Locate every blood parasite and identify its species.
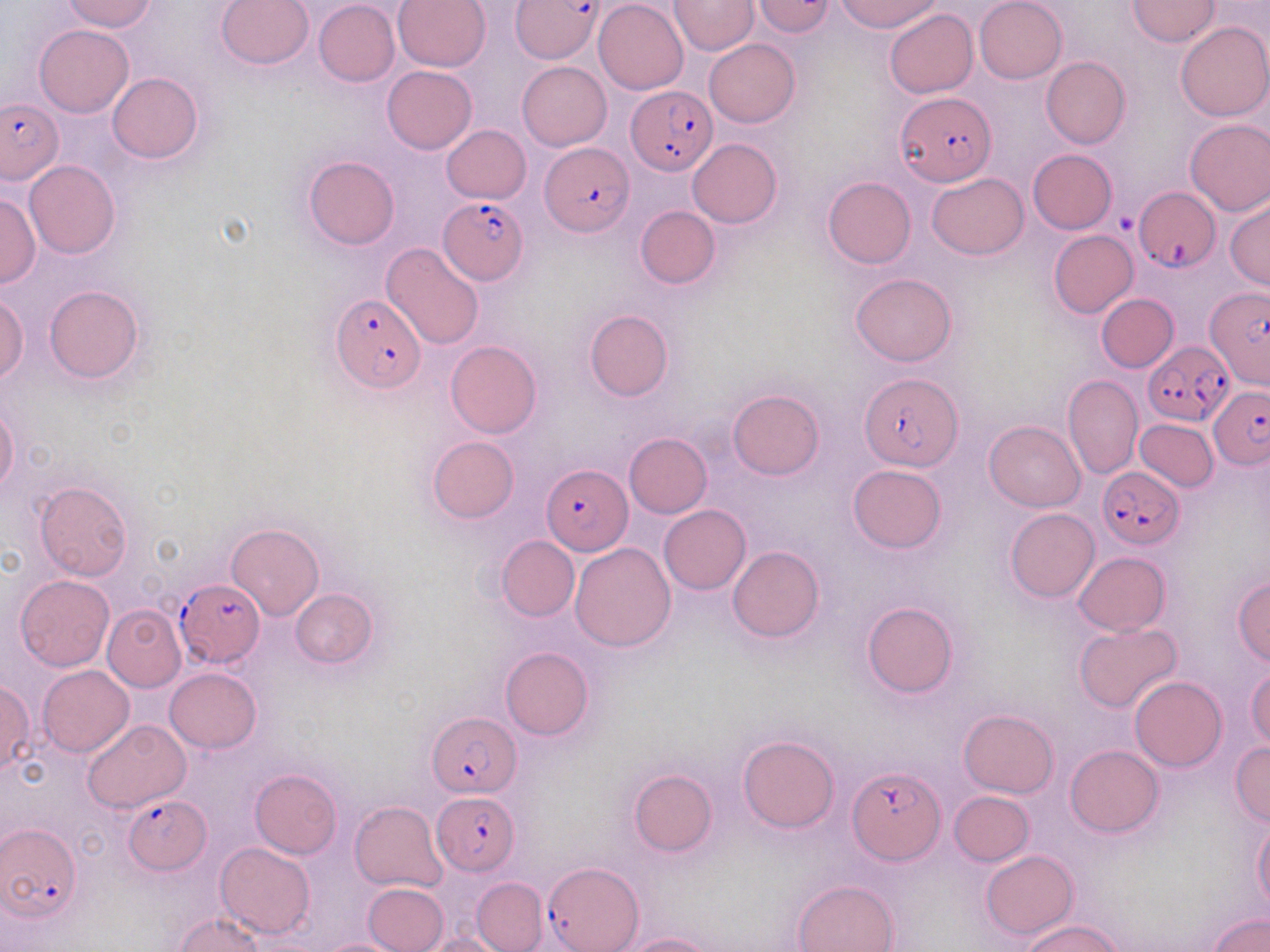
Approximate bounding boxes as (x1, y1, x2, y2) in pixels.
Plasmodium falciparum-infected red blood cells: (511, 0, 601, 63), (626, 87, 715, 176), (895, 93, 995, 187), (0, 97, 63, 185), (541, 142, 633, 237), (1135, 190, 1221, 274), (442, 194, 529, 283), (1204, 285, 1270, 392), (329, 294, 424, 392), (1143, 342, 1234, 425), (859, 373, 963, 471), (1210, 387, 1270, 469), (544, 462, 631, 557), (1098, 467, 1184, 549), (175, 579, 265, 667), (427, 711, 520, 794), (848, 766, 946, 864), (431, 790, 521, 874), (124, 794, 211, 872), (0, 821, 80, 924), (542, 863, 643, 952).
No Plasmodium ovale, Plasmodium malariae, Plasmodium vivax, Babesia divergens, or Trypanosoma brucei observed.

Platelet locations: (1115, 212, 1137, 233). Uninfected red blood cell locations: (61, 0, 157, 33), (216, 0, 314, 71), (594, 0, 687, 94), (668, 0, 759, 56), (751, 0, 836, 37), (834, 0, 944, 34), (975, 0, 1067, 84), (1127, 0, 1219, 46), (313, 1, 400, 86), (392, 1, 490, 72), (885, 9, 978, 98), (1175, 22, 1270, 121), (34, 24, 133, 118), (705, 38, 799, 128), (1041, 56, 1130, 149), (517, 61, 612, 151), (382, 66, 476, 153), (108, 72, 202, 164), (1184, 118, 1270, 215), (442, 124, 531, 203), (688, 138, 781, 228), (1027, 149, 1117, 233), (304, 155, 399, 249), (23, 160, 120, 260), (927, 173, 1028, 259), (823, 176, 916, 269), (0, 193, 41, 288), (1225, 198, 1269, 289), (635, 206, 720, 289), (1048, 231, 1139, 318), (381, 243, 485, 350), (851, 272, 957, 365), (45, 285, 143, 384), (0, 293, 29, 385), (1096, 293, 1179, 372), (585, 310, 674, 400), (446, 341, 542, 438), (1064, 374, 1143, 480), (728, 389, 823, 480), (0, 400, 21, 497), (1135, 419, 1219, 492), (984, 420, 1086, 511), (624, 432, 713, 517), (427, 436, 520, 524), (847, 464, 947, 554), (34, 482, 133, 581), (659, 504, 750, 594), (1005, 508, 1099, 602), (226, 522, 324, 621), (496, 535, 579, 622), (570, 543, 676, 651), (728, 546, 823, 642), (1072, 551, 1170, 636), (16, 574, 113, 671), (1233, 576, 1270, 666), (289, 589, 380, 668), (861, 601, 957, 698), (102, 605, 185, 691), (1073, 622, 1183, 713), (500, 647, 594, 739), (37, 664, 133, 756), (1246, 666, 1270, 749), (164, 667, 261, 753), (1130, 677, 1226, 772), (0, 680, 34, 777), (958, 708, 1059, 798), (82, 720, 192, 813), (738, 735, 839, 833), (1230, 741, 1269, 827), (1066, 744, 1163, 836), (628, 768, 716, 855), (250, 769, 342, 859), (949, 791, 1033, 866), (350, 801, 449, 892), (1254, 820, 1270, 914), (214, 842, 316, 939), (980, 849, 1078, 939), (472, 877, 546, 952), (793, 878, 899, 952), (361, 883, 448, 952), (1208, 913, 1270, 952), (174, 914, 263, 952), (1020, 919, 1125, 952), (421, 932, 508, 952), (618, 933, 721, 952), (313, 937, 412, 952). Slide-level diagnosis: Plasmodium falciparum. 1000x magnification. May-Grünwald-Giemsa stain. Thin blood film. One field of a larger specimen. Optical microscopy. Image is 1270×952 pixels.